Give the extent of all Plasmodium falciparum-infected red blood cells.
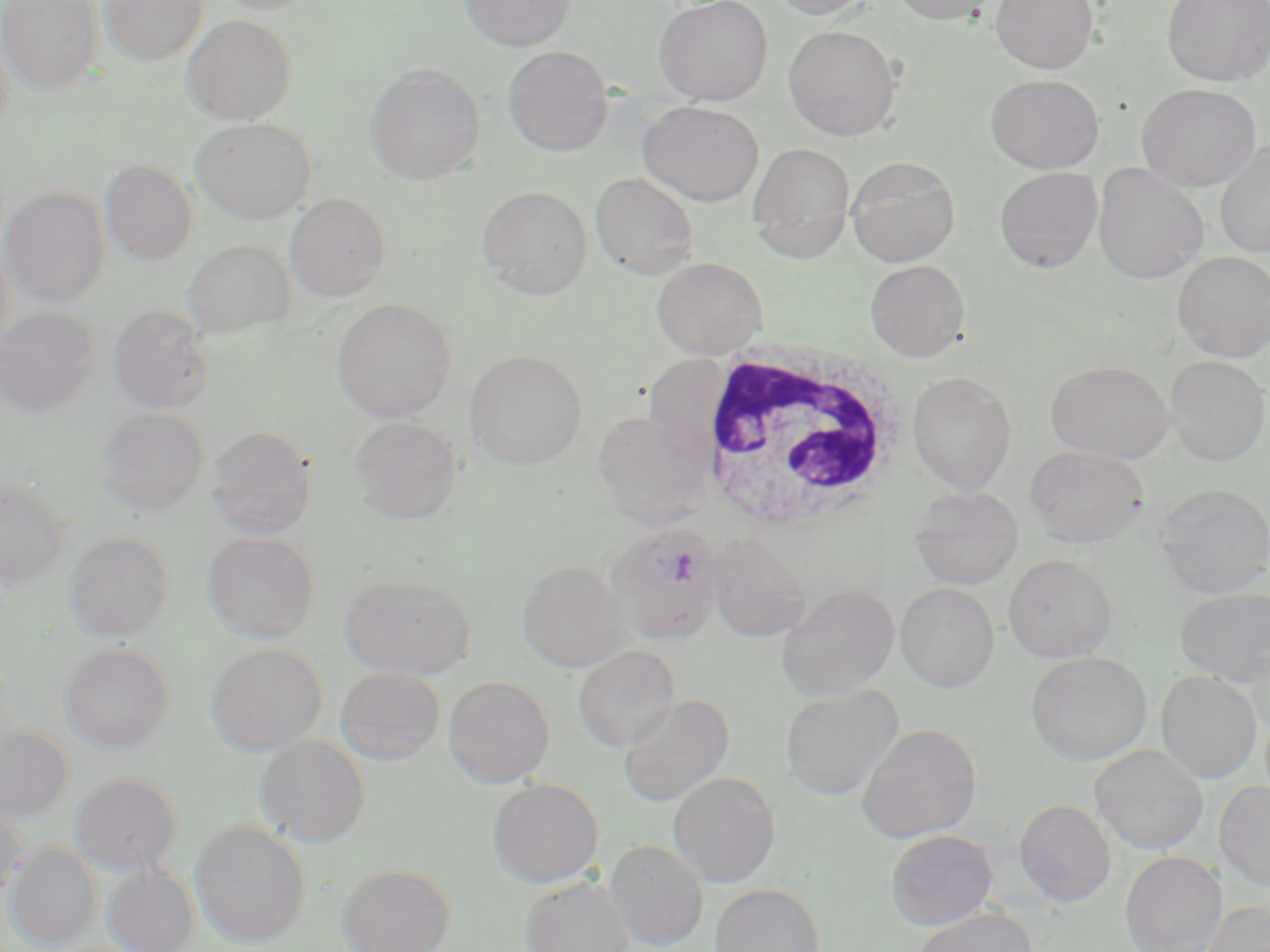
Approximate bounding boxes as named x1/y1/x2/y2 corners in pixels.
Plasmodium falciparum-infected red blood cells: (x1=605, y1=522, x2=726, y2=646).

White blood cell locations: (x1=692, y1=339, x2=910, y2=532). Uninfected red blood cell locations: (x1=1, y1=0, x2=103, y2=94), (x1=100, y1=0, x2=207, y2=64), (x1=208, y1=0, x2=318, y2=15), (x1=459, y1=0, x2=575, y2=51), (x1=654, y1=0, x2=773, y2=104), (x1=769, y1=0, x2=876, y2=19), (x1=888, y1=0, x2=1002, y2=25), (x1=991, y1=0, x2=1098, y2=73), (x1=1163, y1=0, x2=1270, y2=86), (x1=182, y1=14, x2=297, y2=125), (x1=783, y1=25, x2=902, y2=141), (x1=0, y1=26, x2=14, y2=141), (x1=502, y1=45, x2=614, y2=157), (x1=364, y1=63, x2=485, y2=184), (x1=985, y1=74, x2=1104, y2=174), (x1=1137, y1=83, x2=1262, y2=191), (x1=637, y1=101, x2=764, y2=207), (x1=191, y1=117, x2=315, y2=224), (x1=1215, y1=139, x2=1270, y2=258), (x1=747, y1=143, x2=856, y2=261), (x1=846, y1=156, x2=960, y2=267), (x1=100, y1=159, x2=197, y2=266), (x1=1093, y1=163, x2=1209, y2=283), (x1=994, y1=167, x2=1103, y2=273), (x1=590, y1=173, x2=699, y2=279), (x1=477, y1=185, x2=593, y2=299), (x1=1, y1=187, x2=109, y2=307), (x1=285, y1=194, x2=391, y2=302), (x1=0, y1=235, x2=14, y2=352), (x1=183, y1=240, x2=295, y2=337), (x1=1172, y1=251, x2=1270, y2=362), (x1=652, y1=256, x2=767, y2=358), (x1=865, y1=259, x2=969, y2=361), (x1=332, y1=299, x2=456, y2=423), (x1=108, y1=305, x2=215, y2=414), (x1=0, y1=308, x2=97, y2=417), (x1=464, y1=349, x2=587, y2=470), (x1=638, y1=354, x2=739, y2=480), (x1=1165, y1=356, x2=1269, y2=467), (x1=1046, y1=361, x2=1174, y2=463), (x1=907, y1=371, x2=1017, y2=493), (x1=97, y1=408, x2=210, y2=516), (x1=592, y1=410, x2=713, y2=528), (x1=349, y1=416, x2=462, y2=525), (x1=206, y1=425, x2=317, y2=540), (x1=1025, y1=445, x2=1149, y2=548), (x1=0, y1=481, x2=69, y2=590), (x1=1154, y1=483, x2=1270, y2=598), (x1=909, y1=487, x2=1023, y2=590), (x1=64, y1=531, x2=173, y2=641), (x1=202, y1=532, x2=319, y2=642), (x1=704, y1=533, x2=812, y2=642), (x1=1003, y1=554, x2=1117, y2=662), (x1=517, y1=560, x2=630, y2=673), (x1=340, y1=574, x2=477, y2=679), (x1=895, y1=582, x2=1000, y2=692), (x1=777, y1=584, x2=899, y2=701), (x1=1175, y1=586, x2=1270, y2=686), (x1=59, y1=643, x2=174, y2=753), (x1=205, y1=643, x2=327, y2=755), (x1=573, y1=645, x2=680, y2=752), (x1=1026, y1=651, x2=1152, y2=765), (x1=335, y1=667, x2=445, y2=765), (x1=1156, y1=670, x2=1262, y2=784), (x1=444, y1=676, x2=555, y2=787), (x1=780, y1=685, x2=902, y2=801), (x1=617, y1=694, x2=734, y2=808), (x1=856, y1=723, x2=982, y2=843), (x1=0, y1=726, x2=72, y2=824), (x1=254, y1=734, x2=370, y2=847), (x1=1090, y1=743, x2=1209, y2=854), (x1=1112, y1=745, x2=1219, y2=952), (x1=668, y1=771, x2=781, y2=887), (x1=70, y1=772, x2=182, y2=875), (x1=487, y1=778, x2=604, y2=887), (x1=1215, y1=780, x2=1270, y2=892), (x1=1015, y1=799, x2=1116, y2=906), (x1=0, y1=803, x2=26, y2=900), (x1=191, y1=819, x2=311, y2=948), (x1=885, y1=830, x2=997, y2=930), (x1=606, y1=839, x2=708, y2=950), (x1=7, y1=843, x2=100, y2=949), (x1=1120, y1=851, x2=1226, y2=952), (x1=337, y1=863, x2=455, y2=952), (x1=104, y1=864, x2=199, y2=952), (x1=520, y1=875, x2=634, y2=952), (x1=710, y1=883, x2=824, y2=952), (x1=1203, y1=900, x2=1270, y2=952), (x1=913, y1=906, x2=1038, y2=952). Slide-level diagnosis: Plasmodium falciparum. Captured at 1000x magnification. May-Grünwald-Giemsa stain. Thin blood smear. Optical microscopy. Single field of view. Image is 1270×952 pixels.